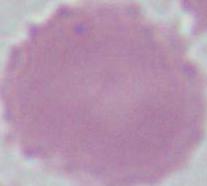
Captured at 1000x magnification. Photomicrograph. A red blood cell is shown.